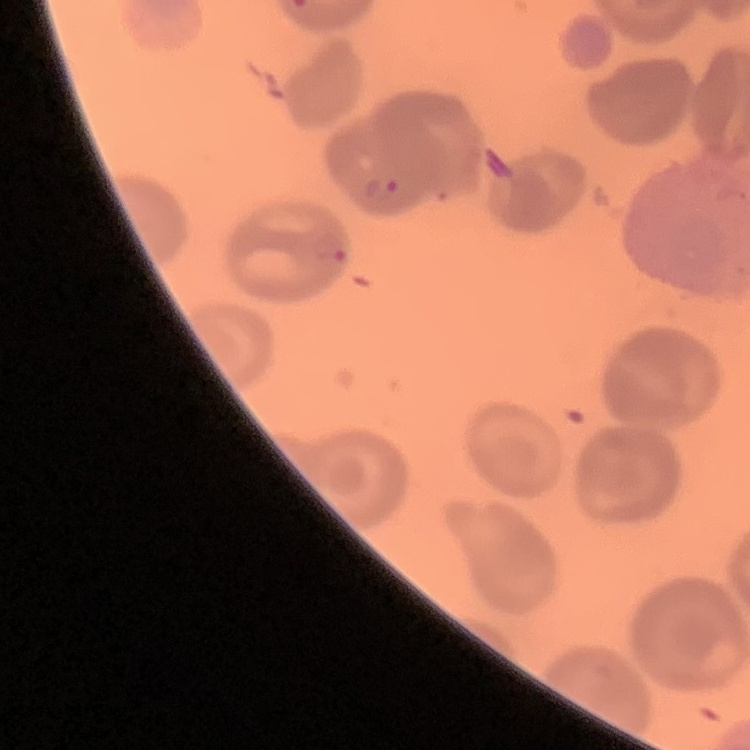
erythrocyte morphology = no rouleaux formation
preparation = thin blood smear
stain = Field's or Giemsa
image type = one tile cut from a larger photomicrograph